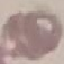 Malaria status: uninfected. Giemsa stain. Cell patch, automatically extracted from a larger field of view and resized to 64 × 64 pixels. Thin blood smear. Photographed with a smartphone camera at the microscope eyepiece.